Locate every blood parasite and identify its species.
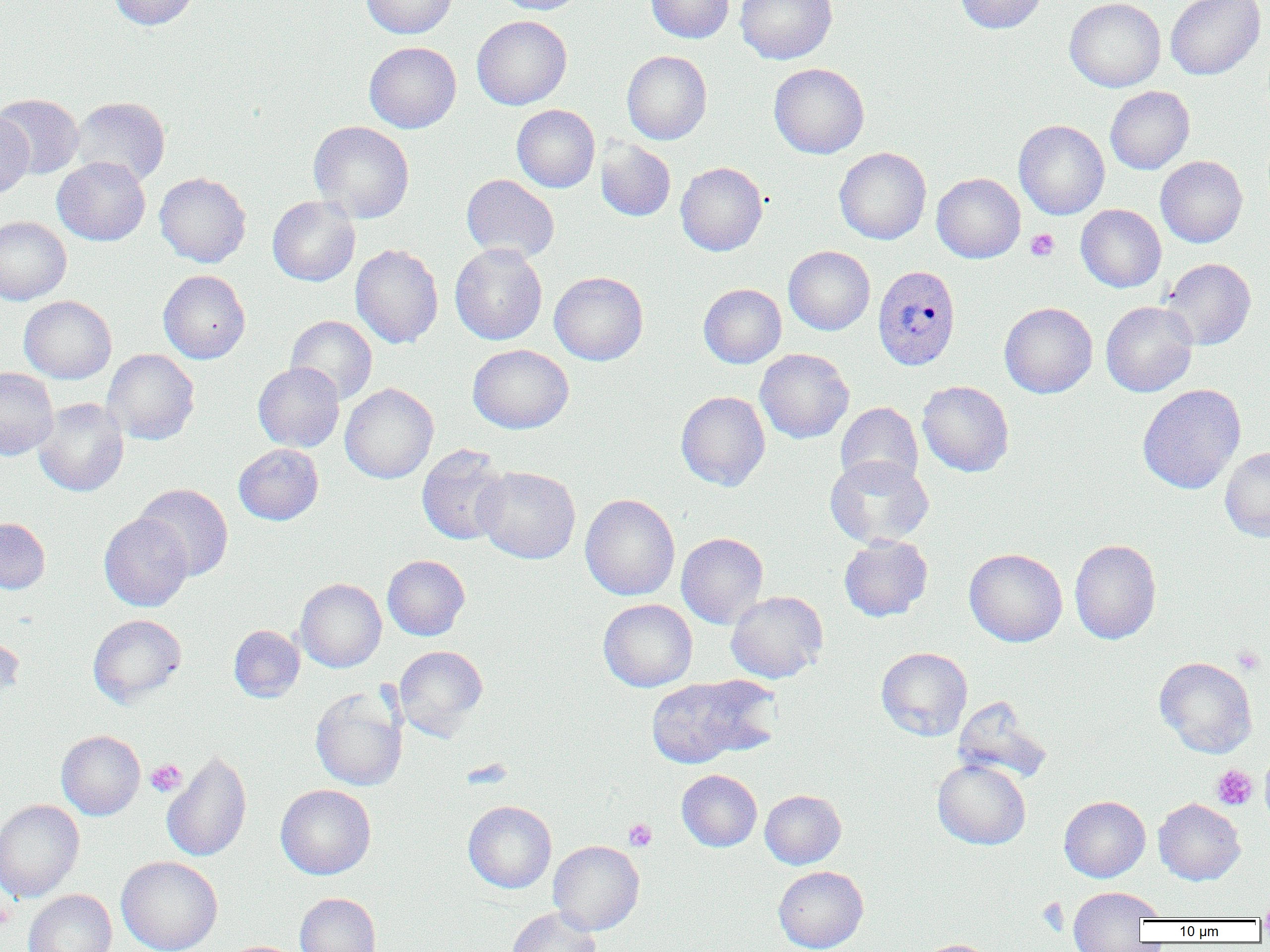
Approximate bounding boxes as (x1, y1, x2, y2) in pixels.
Plasmodium vivax-infected red blood cells: (872, 264, 961, 371).
No Plasmodium falciparum, Plasmodium ovale, Plasmodium malariae, Babesia divergens, or Trypanosoma brucei observed.

slide_level_diagnosis: Plasmodium vivax
image_size: 1270×952 pixels
uninfected_red_blood_cell_locations: 'approximate bounding boxes as (x1, y1, x2, y2) in pixels: (108, 0, 200, 30), (361, 0, 457, 38), (493, 0, 589, 14), (646, 0, 734, 43), (735, 0, 837, 64), (955, 0, 1048, 34), (1065, 0, 1166, 92), (1165, 0, 1266, 80), (472, 15, 572, 110), (364, 42, 461, 133), (621, 51, 712, 144), (769, 63, 869, 158), (1105, 86, 1195, 174), (0, 93, 84, 179), (70, 96, 170, 187), (512, 104, 600, 192), (0, 113, 34, 201), (308, 120, 415, 223), (1014, 120, 1109, 220), (596, 138, 676, 221), (834, 147, 931, 245), (52, 156, 151, 246), (1156, 156, 1247, 247), (676, 162, 767, 256), (154, 172, 251, 267), (932, 172, 1026, 263), (461, 174, 559, 263), (267, 196, 360, 286), (1076, 204, 1166, 292), (0, 216, 71, 305), (450, 243, 548, 345), (351, 244, 443, 348), (784, 246, 875, 335), (1161, 258, 1256, 350), (158, 270, 250, 363), (549, 271, 648, 365), (698, 283, 787, 368), (18, 295, 117, 384), (1101, 301, 1198, 397), (999, 302, 1098, 398), (286, 315, 377, 405), (467, 344, 574, 434), (755, 348, 854, 443), (102, 349, 200, 445), (253, 362, 345, 452), (0, 368, 58, 459), (917, 380, 1014, 476), (340, 383, 438, 484), (1137, 384, 1246, 494), (676, 391, 771, 491), (33, 398, 129, 497), (836, 402, 923, 490), (233, 444, 323, 525), (416, 444, 511, 546), (1220, 447, 1270, 542), (825, 455, 934, 548), (474, 465, 581, 564), (135, 483, 233, 581), (580, 494, 680, 600), (99, 513, 193, 611), (0, 517, 50, 594), (676, 532, 769, 628), (838, 535, 932, 621), (1069, 539, 1161, 644), (964, 548, 1067, 647), (383, 555, 470, 640), (295, 578, 387, 672), (726, 591, 828, 683), (598, 598, 697, 692), (88, 613, 187, 707), (228, 625, 305, 702), (0, 633, 24, 708), (394, 645, 488, 738), (876, 647, 973, 740), (1154, 656, 1257, 758), (645, 675, 774, 767), (310, 688, 408, 791), (952, 696, 1053, 785), (56, 730, 145, 820), (162, 749, 252, 862), (1260, 754, 1270, 827), (932, 759, 1031, 850), (677, 770, 762, 851), (276, 784, 376, 879), (760, 790, 846, 869), (1059, 795, 1150, 882), (1154, 798, 1245, 885), (0, 799, 85, 903), (463, 800, 557, 893), (548, 840, 644, 935), (116, 856, 222, 952), (773, 866, 868, 952), (1069, 886, 1160, 950), (23, 889, 117, 952), (1258, 890, 1270, 926), (295, 892, 381, 952), (506, 907, 602, 952), (916, 939, 997, 952)'
magnification: 1000x
platelet_locations: 'approximate bounding boxes as (x1, y1, x2, y2) in pixels: (1026, 229, 1059, 261), (1232, 645, 1265, 674), (145, 759, 187, 797), (1212, 764, 1257, 810), (623, 818, 657, 851), (0, 897, 15, 932), (1038, 897, 1069, 935)'
preparation: thin blood film
modality: optical microscopy
field_of_view: one of a larger specimen